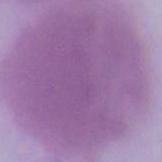

modality = photomicrograph
magnification = 1000x
identification = red blood cell